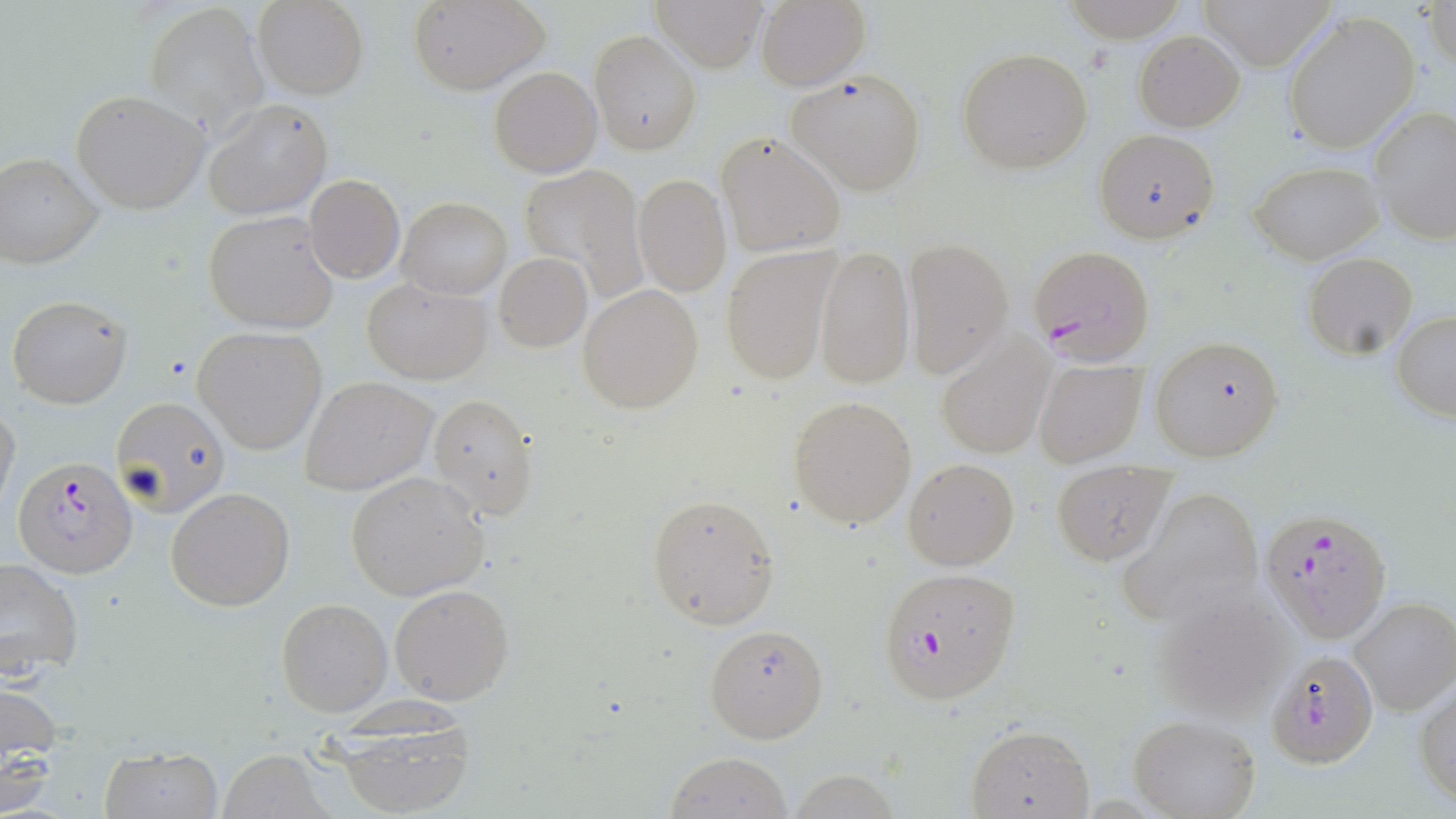
slide-level diagnosis = Plasmodium falciparum
stain = May-Grünwald-Giemsa
preparation = thin blood film
field of view = single
image size = 1456×819 pixels
modality = optical microscopy
uninfected red blood cell locations = approximate bounding boxes as named x1/y1/x2/y2 corners in pixels: (x1=409, y1=0, x2=549, y2=94), (x1=651, y1=0, x2=769, y2=72), (x1=755, y1=0, x2=870, y2=91), (x1=1062, y1=0, x2=1186, y2=41), (x1=1194, y1=0, x2=1338, y2=70), (x1=253, y1=1, x2=368, y2=99), (x1=145, y1=2, x2=266, y2=133), (x1=1425, y1=2, x2=1455, y2=74), (x1=1281, y1=11, x2=1421, y2=154), (x1=590, y1=30, x2=700, y2=156), (x1=1134, y1=32, x2=1244, y2=131), (x1=957, y1=47, x2=1094, y2=174), (x1=489, y1=65, x2=602, y2=178), (x1=788, y1=68, x2=926, y2=195), (x1=71, y1=90, x2=209, y2=213), (x1=203, y1=101, x2=332, y2=219), (x1=1369, y1=105, x2=1456, y2=245), (x1=1093, y1=128, x2=1219, y2=243), (x1=717, y1=131, x2=845, y2=256), (x1=0, y1=153, x2=103, y2=270), (x1=1249, y1=160, x2=1382, y2=263), (x1=519, y1=165, x2=644, y2=288), (x1=634, y1=174, x2=731, y2=295), (x1=304, y1=175, x2=404, y2=282), (x1=398, y1=197, x2=511, y2=299), (x1=204, y1=209, x2=342, y2=333), (x1=903, y1=238, x2=1014, y2=376), (x1=814, y1=244, x2=913, y2=390), (x1=721, y1=246, x2=837, y2=383), (x1=1302, y1=253, x2=1418, y2=358), (x1=494, y1=254, x2=592, y2=351), (x1=363, y1=277, x2=492, y2=383), (x1=578, y1=285, x2=705, y2=414), (x1=6, y1=293, x2=132, y2=408), (x1=1391, y1=310, x2=1456, y2=421), (x1=194, y1=327, x2=328, y2=454), (x1=937, y1=335, x2=1054, y2=457), (x1=1150, y1=335, x2=1284, y2=460), (x1=1033, y1=358, x2=1147, y2=468), (x1=302, y1=376, x2=437, y2=495), (x1=427, y1=395, x2=538, y2=520), (x1=111, y1=396, x2=229, y2=517), (x1=788, y1=396, x2=916, y2=529), (x1=0, y1=402, x2=21, y2=521), (x1=902, y1=458, x2=1019, y2=570), (x1=1051, y1=463, x2=1176, y2=565), (x1=346, y1=472, x2=490, y2=600), (x1=165, y1=487, x2=294, y2=611), (x1=1116, y1=489, x2=1266, y2=629), (x1=646, y1=493, x2=779, y2=628), (x1=0, y1=556, x2=84, y2=681), (x1=390, y1=583, x2=515, y2=705), (x1=1147, y1=583, x2=1296, y2=723), (x1=276, y1=598, x2=392, y2=717), (x1=1349, y1=598, x2=1456, y2=716), (x1=704, y1=622, x2=829, y2=744), (x1=1265, y1=651, x2=1378, y2=770), (x1=0, y1=683, x2=62, y2=810), (x1=1415, y1=685, x2=1456, y2=806), (x1=1128, y1=715, x2=1260, y2=819), (x1=964, y1=722, x2=1094, y2=818), (x1=326, y1=723, x2=480, y2=819), (x1=98, y1=744, x2=221, y2=819), (x1=219, y1=750, x2=329, y2=818), (x1=665, y1=752, x2=792, y2=818), (x1=787, y1=769, x2=903, y2=819)
magnification = 1000x
Plasmodium falciparum-infected red blood cell locations = approximate bounding boxes as named x1/y1/x2/y2 corners in pixels: (x1=1027, y1=246, x2=1154, y2=363), (x1=13, y1=454, x2=138, y2=577), (x1=1262, y1=508, x2=1394, y2=644), (x1=876, y1=566, x2=1021, y2=704)